Assess this cell for malaria.
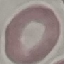
It is uninfected.

preparation: thin smear
image_type: automatically extracted cell patch, resized to 64 × 64 pixels
stain: Giemsa
capture: smartphone camera at the microscope eyepiece